Name the cell type shown.
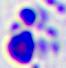
A leukocyte.

Summary:
  - Magnification: 400x
  - Modality: micrograph